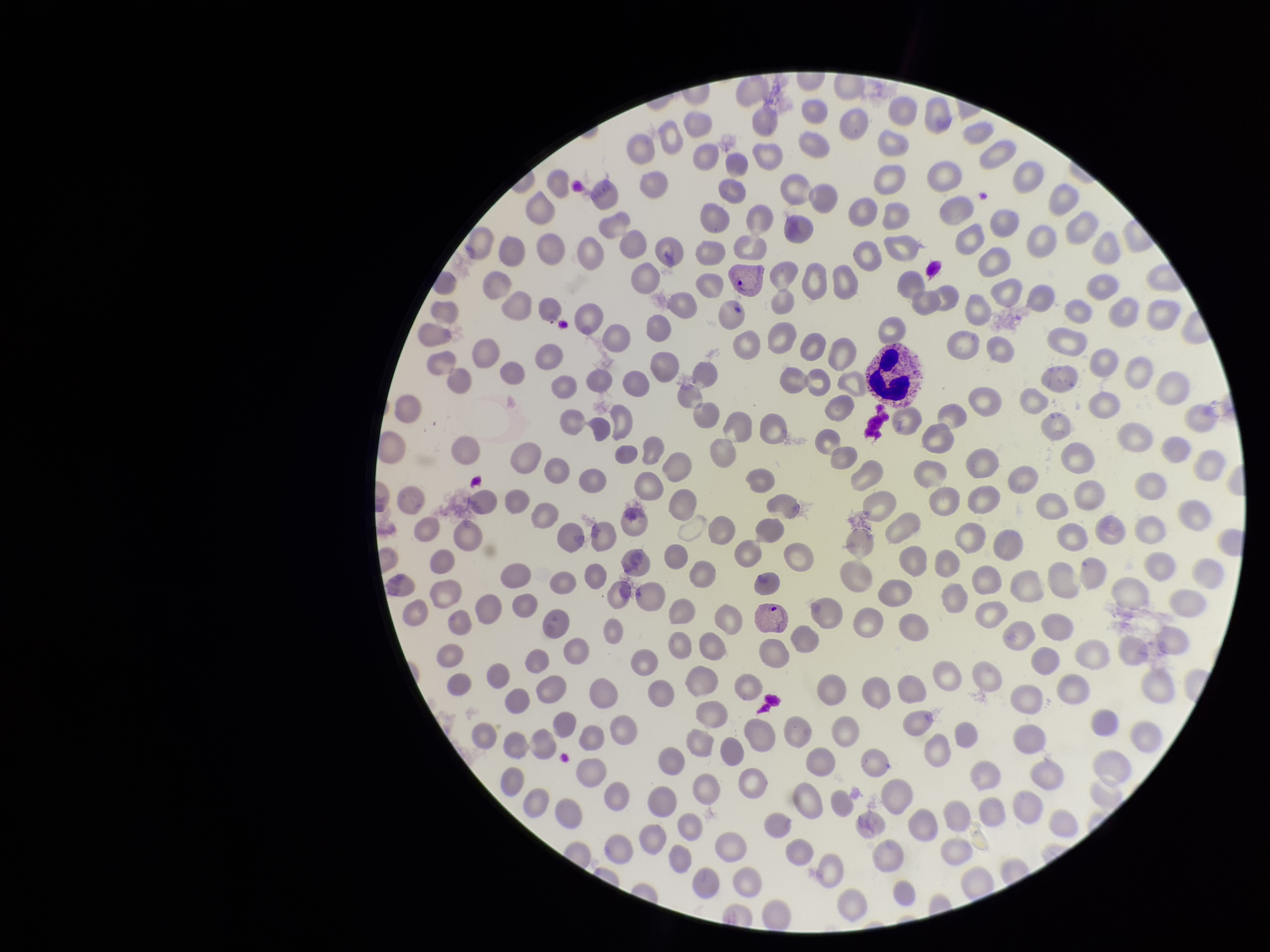 Species reported for this patient: Plasmodium vivax. Giemsa stain. Parasitized red blood cells: seen. Smartphone photograph taken through the eyepiece of a microscope. Red blood cell count: 269. Image is 1270×952 pixels. Parasitized red blood cell count: 2. Patient malaria status: positive. Preparation: thin. One field from this slide.